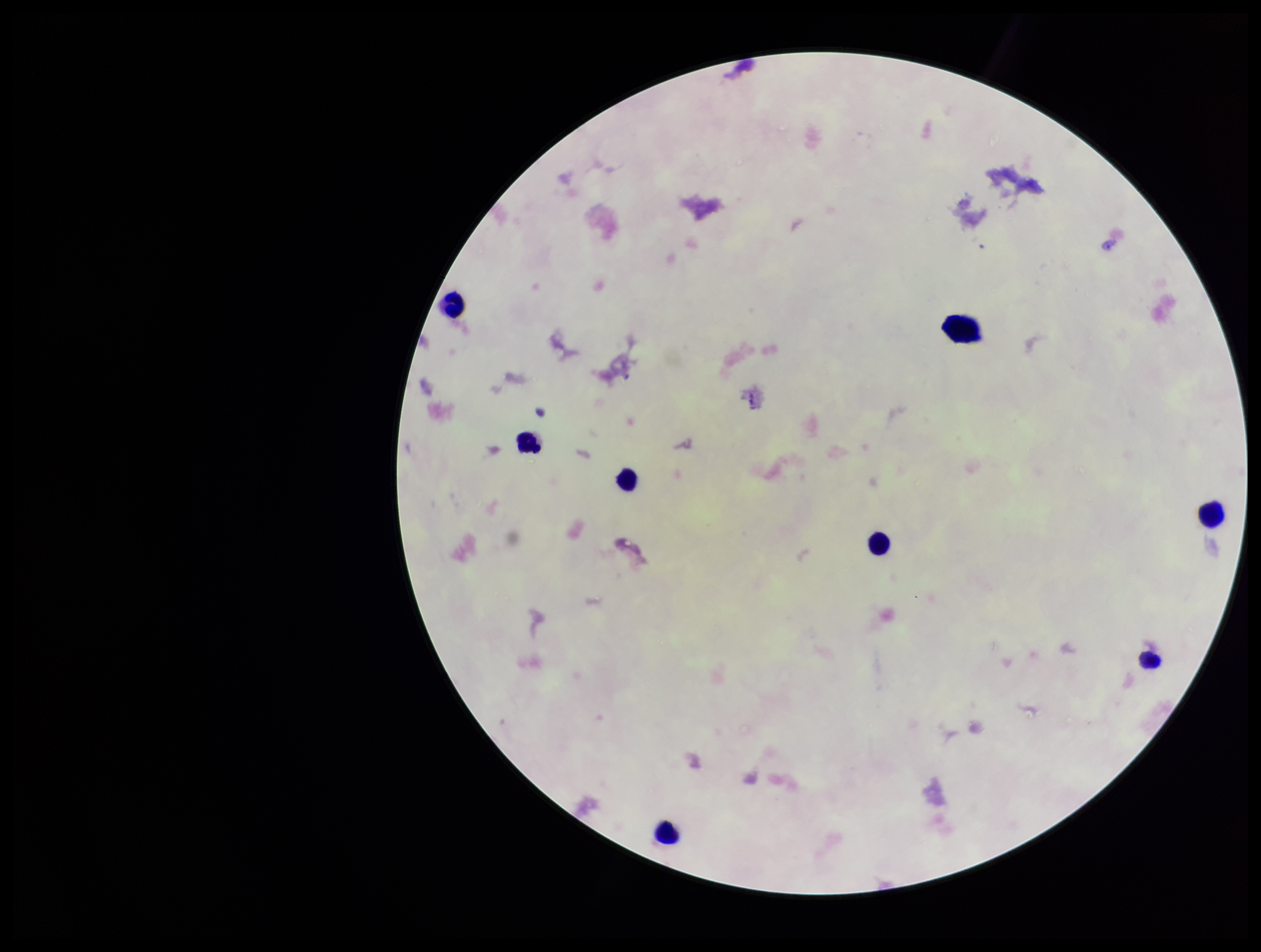

field_of_view: one from this slide
image_size: 1261×952 pixels
patient_malaria_status: negative
stain: Giemsa
parasite_count: 0
leukocyte_count: 7
capture: smartphone photograph through the microscope eyepiece
plasmodium_parasites: none identified
preparation: thick smear